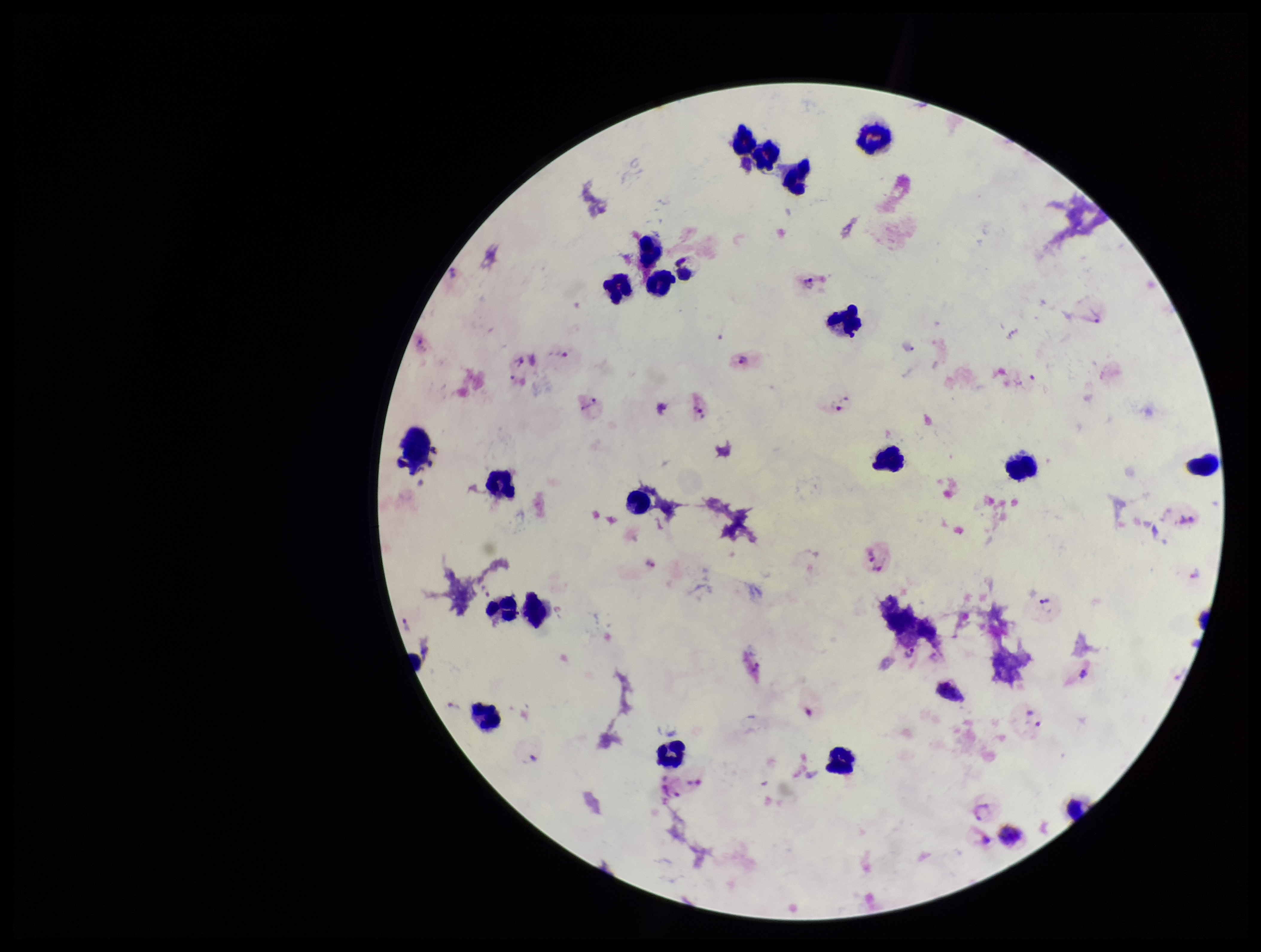

Plasmodium parasites = identified
preparation = thick smear
stain = Giemsa
capture = smartphone photograph through the microscope eyepiece
image size = 1261×952 pixels
parasite count = 10
patient malaria status = positive
field of view = one from this slide
leukocyte count = 21
species reported for this patient = Plasmodium vivax